Name the parasite shown.
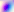

This is Toxoplasma gondii.

Micrograph. 400x magnification.